Outline each blood parasite and name the species.
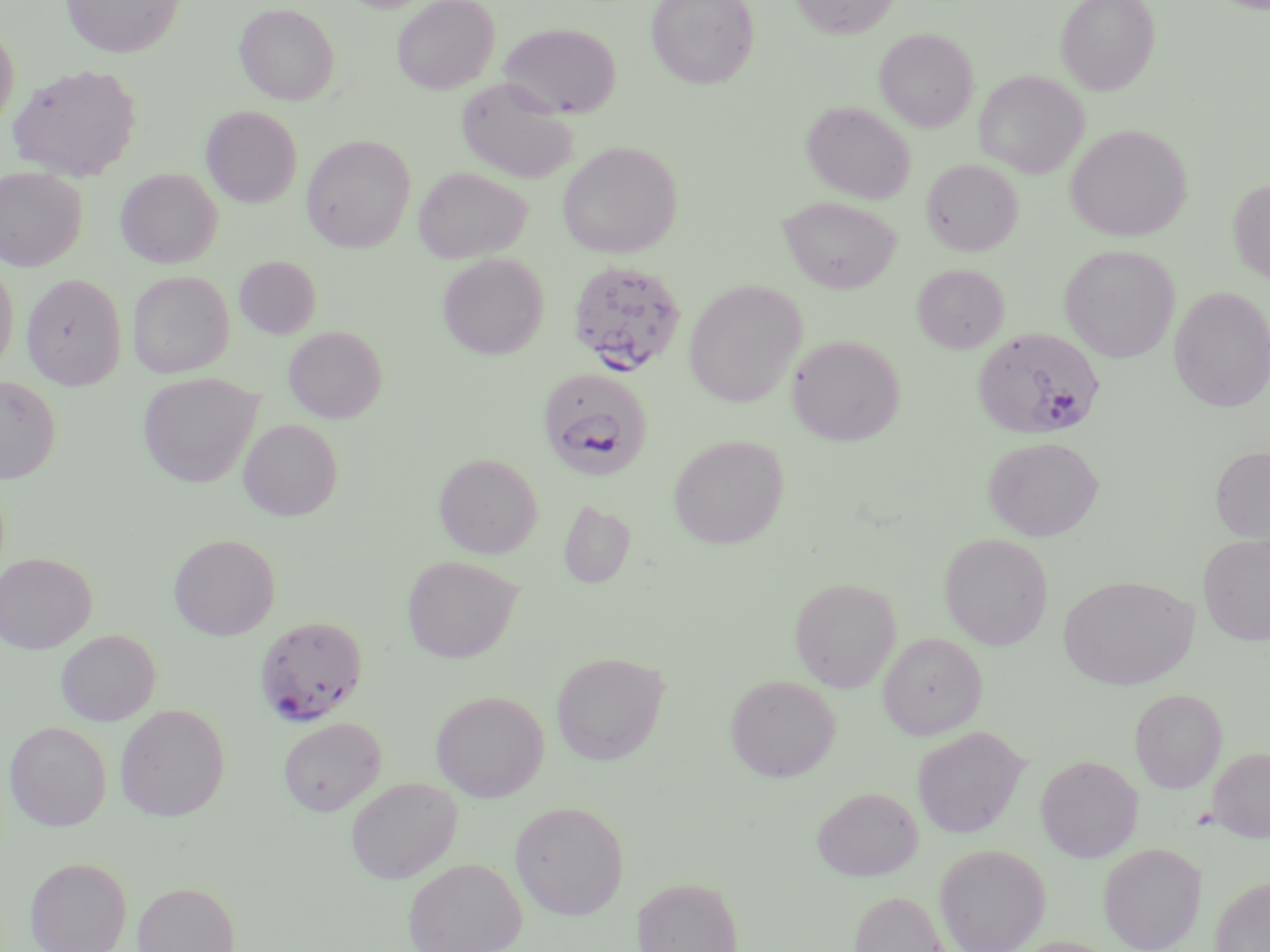

Approximate bounding boxes as (x1, y1, x2, y2) in pixels.
Plasmodium falciparum-infected red blood cells: (567, 262, 688, 378), (972, 328, 1106, 440), (536, 367, 653, 479), (254, 615, 369, 726).
No Plasmodium ovale, Plasmodium malariae, Plasmodium vivax, Babesia divergens, or Trypanosoma brucei observed.

{
  "slide_level_diagnosis": "Plasmodium falciparum",
  "field_of_view": "single",
  "image_size": "1270×952 pixels",
  "stain": "May-Grünwald-Giemsa",
  "magnification": "1000x",
  "preparation": "thin blood smear",
  "modality": "light microscopy",
  "uninfected_red_blood_cell_locations": "approximate bounding boxes as (x1, y1, x2, y2) in pixels: (61, 0, 184, 58), (392, 0, 499, 94), (646, 0, 759, 89), (790, 0, 900, 38), (1057, 0, 1159, 95), (234, 3, 340, 105), (0, 22, 20, 131), (500, 23, 621, 119), (875, 28, 979, 132), (8, 63, 142, 181), (975, 70, 1088, 177), (456, 78, 578, 183), (802, 101, 916, 204), (201, 105, 303, 207), (1065, 124, 1192, 242), (302, 134, 416, 252), (557, 141, 683, 258), (922, 159, 1022, 256), (413, 166, 532, 264), (0, 167, 88, 270), (115, 168, 222, 268), (1228, 179, 1270, 284), (779, 196, 902, 293), (1059, 245, 1180, 363), (437, 252, 549, 359), (234, 255, 322, 339), (0, 259, 19, 372), (912, 263, 1010, 353), (128, 270, 234, 378), (22, 273, 127, 388), (684, 280, 807, 407), (1168, 286, 1270, 412), (284, 325, 387, 422), (786, 334, 905, 446), (138, 373, 263, 488), (0, 376, 62, 483), (238, 418, 343, 521), (669, 434, 789, 549), (983, 436, 1104, 541), (1210, 445, 1270, 543), (434, 452, 542, 558), (558, 499, 636, 589), (1198, 532, 1270, 646), (939, 533, 1054, 650), (169, 534, 281, 640), (0, 552, 96, 653), (402, 555, 523, 662), (1058, 574, 1198, 690), (789, 576, 901, 692), (56, 629, 160, 726), (878, 633, 987, 739), (551, 651, 670, 765), (725, 674, 840, 782), (1130, 688, 1227, 792), (431, 690, 549, 802), (115, 703, 230, 821), (278, 717, 386, 816), (4, 720, 111, 831), (912, 726, 1029, 839), (1207, 747, 1270, 842), (1036, 755, 1143, 862), (346, 777, 462, 883), (811, 786, 923, 881), (510, 801, 629, 919), (1098, 842, 1206, 951), (934, 844, 1050, 952), (24, 856, 132, 952), (402, 857, 526, 952), (632, 876, 743, 952), (1210, 876, 1270, 952), (132, 881, 241, 952), (848, 890, 951, 952), (1005, 936, 1121, 952)"
}